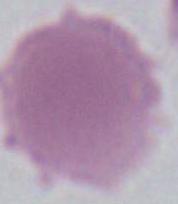 Micrograph. Captured at 1000x magnification. An erythrocyte is seen.